Assess this cell for malaria.
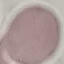
Uninfected.

Summary:
  - Stain: Giemsa
  - Preparation: thin blood smear
  - Image type: cell patch, automatically extracted from a larger field of view and resized to 64 × 64 pixels
  - Capture: smartphone camera at the microscope eyepiece